Name the blood parasite species.
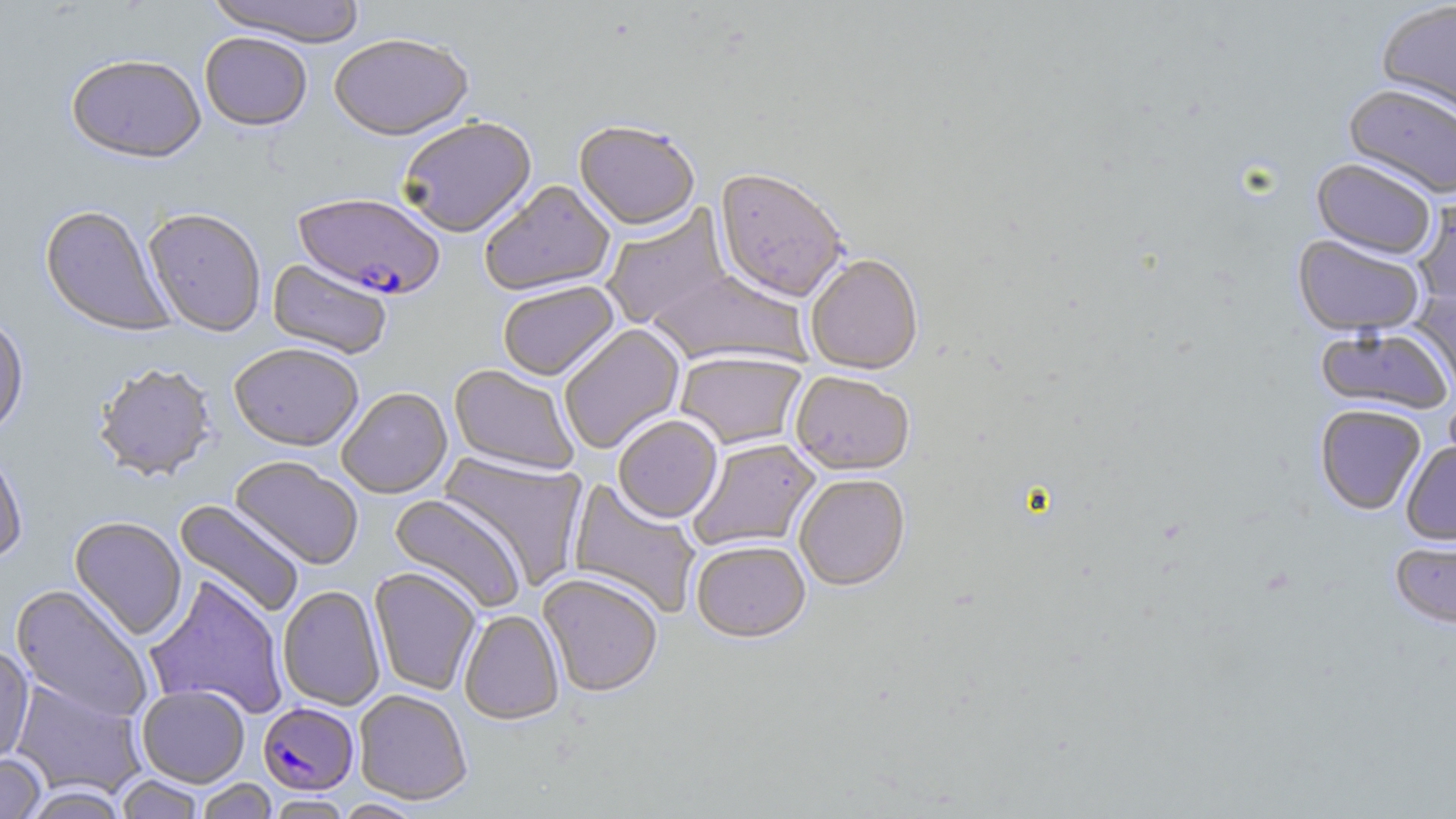
Plasmodium falciparum.

Summary:
  - Coordinate format: approximate bounding boxes as named x1/y1/x2/y2 corners in pixels
  - Uninfected red blood cell locations: (x1=206, y1=0, x2=368, y2=50), (x1=1377, y1=2, x2=1456, y2=122), (x1=199, y1=35, x2=312, y2=134), (x1=329, y1=37, x2=474, y2=145), (x1=66, y1=58, x2=207, y2=167), (x1=1343, y1=82, x2=1456, y2=199), (x1=399, y1=119, x2=538, y2=240), (x1=574, y1=123, x2=700, y2=234), (x1=1312, y1=157, x2=1437, y2=259), (x1=713, y1=171, x2=849, y2=305), (x1=480, y1=181, x2=616, y2=298), (x1=1414, y1=191, x2=1456, y2=309), (x1=601, y1=205, x2=733, y2=330), (x1=39, y1=206, x2=174, y2=338), (x1=143, y1=210, x2=266, y2=339), (x1=1292, y1=234, x2=1426, y2=336), (x1=806, y1=256, x2=923, y2=376), (x1=267, y1=260, x2=392, y2=360), (x1=648, y1=268, x2=811, y2=370), (x1=498, y1=282, x2=620, y2=383), (x1=1411, y1=288, x2=1456, y2=401), (x1=0, y1=317, x2=29, y2=440), (x1=560, y1=325, x2=685, y2=454), (x1=1315, y1=325, x2=1455, y2=416), (x1=228, y1=346, x2=364, y2=454), (x1=675, y1=353, x2=807, y2=451), (x1=93, y1=365, x2=218, y2=484), (x1=448, y1=366, x2=579, y2=477), (x1=791, y1=373, x2=915, y2=478), (x1=337, y1=389, x2=452, y2=499), (x1=1314, y1=404, x2=1426, y2=515), (x1=613, y1=417, x2=723, y2=525), (x1=686, y1=438, x2=822, y2=554), (x1=1401, y1=441, x2=1456, y2=545), (x1=0, y1=448, x2=27, y2=564), (x1=439, y1=453, x2=587, y2=589), (x1=229, y1=457, x2=363, y2=570), (x1=795, y1=475, x2=910, y2=593), (x1=566, y1=477, x2=702, y2=620), (x1=388, y1=493, x2=526, y2=614), (x1=173, y1=499, x2=305, y2=618), (x1=68, y1=517, x2=187, y2=641), (x1=1390, y1=536, x2=1456, y2=630), (x1=691, y1=542, x2=811, y2=646), (x1=369, y1=567, x2=481, y2=696), (x1=144, y1=574, x2=288, y2=720), (x1=538, y1=575, x2=663, y2=699), (x1=10, y1=585, x2=152, y2=725), (x1=277, y1=586, x2=385, y2=712), (x1=459, y1=610, x2=564, y2=727), (x1=0, y1=646, x2=34, y2=766), (x1=10, y1=678, x2=147, y2=799), (x1=138, y1=686, x2=249, y2=788), (x1=354, y1=690, x2=472, y2=806), (x1=0, y1=752, x2=47, y2=818), (x1=115, y1=775, x2=206, y2=819), (x1=194, y1=778, x2=279, y2=819), (x1=18, y1=786, x2=129, y2=818), (x1=266, y1=795, x2=352, y2=818), (x1=334, y1=799, x2=424, y2=818)
  - Plasmodium falciparum-infected red blood cell locations: (x1=292, y1=195, x2=444, y2=303), (x1=258, y1=703, x2=359, y2=796)
  - Image size: 1456×819 pixels
  - Modality: light microscopy
  - Field of view: one of a larger specimen
  - Magnification: 1000x
  - Stain: May-Grünwald-Giemsa
  - Preparation: thin blood smear